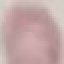
Summary:
  - Malaria status: uninfected
  - Preparation: thin blood film
  - Capture: smartphone through the microscope eyepiece
  - Image type: automatically extracted cell patch, resized to 64 × 64 pixels
  - Stain: Giemsa